Name the cell type shown.
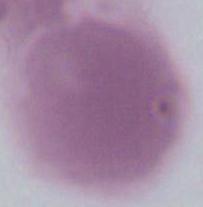

This is an erythrocyte.

modality = photomicrograph
magnification = 1000x